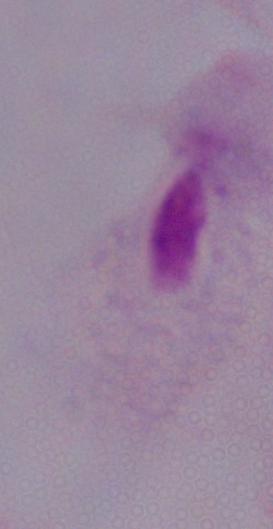 A trichomonad is shown. Micrograph. Captured at 1000x magnification.